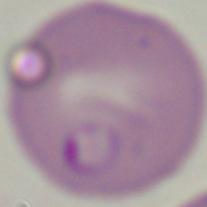 A Babesia parasite is seen. 1000x magnification. Photomicrograph.